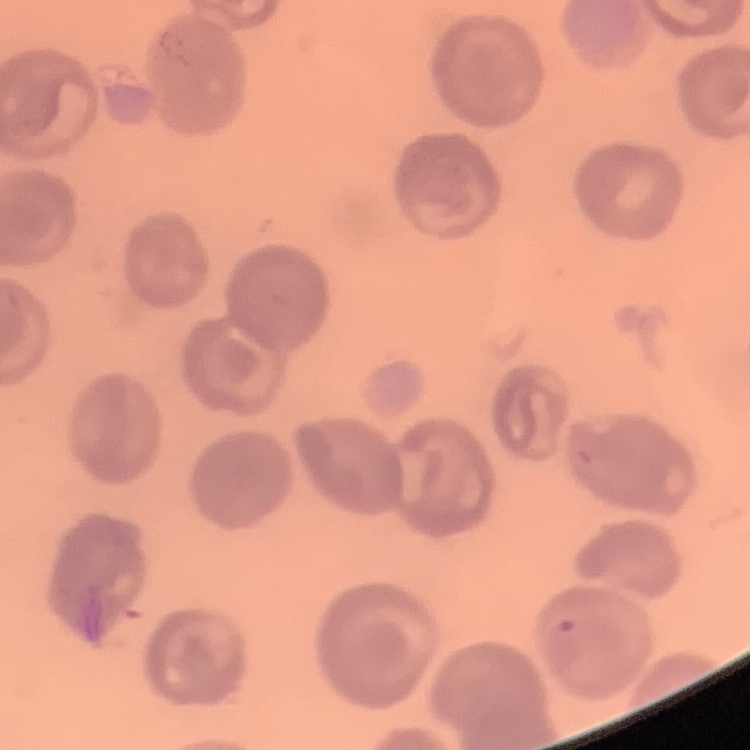

red_blood_cell_morphology: no rouleaux formation
preparation: thin blood film
image_type: one tile cut from a larger photomicrograph
stain: Field's or Giemsa